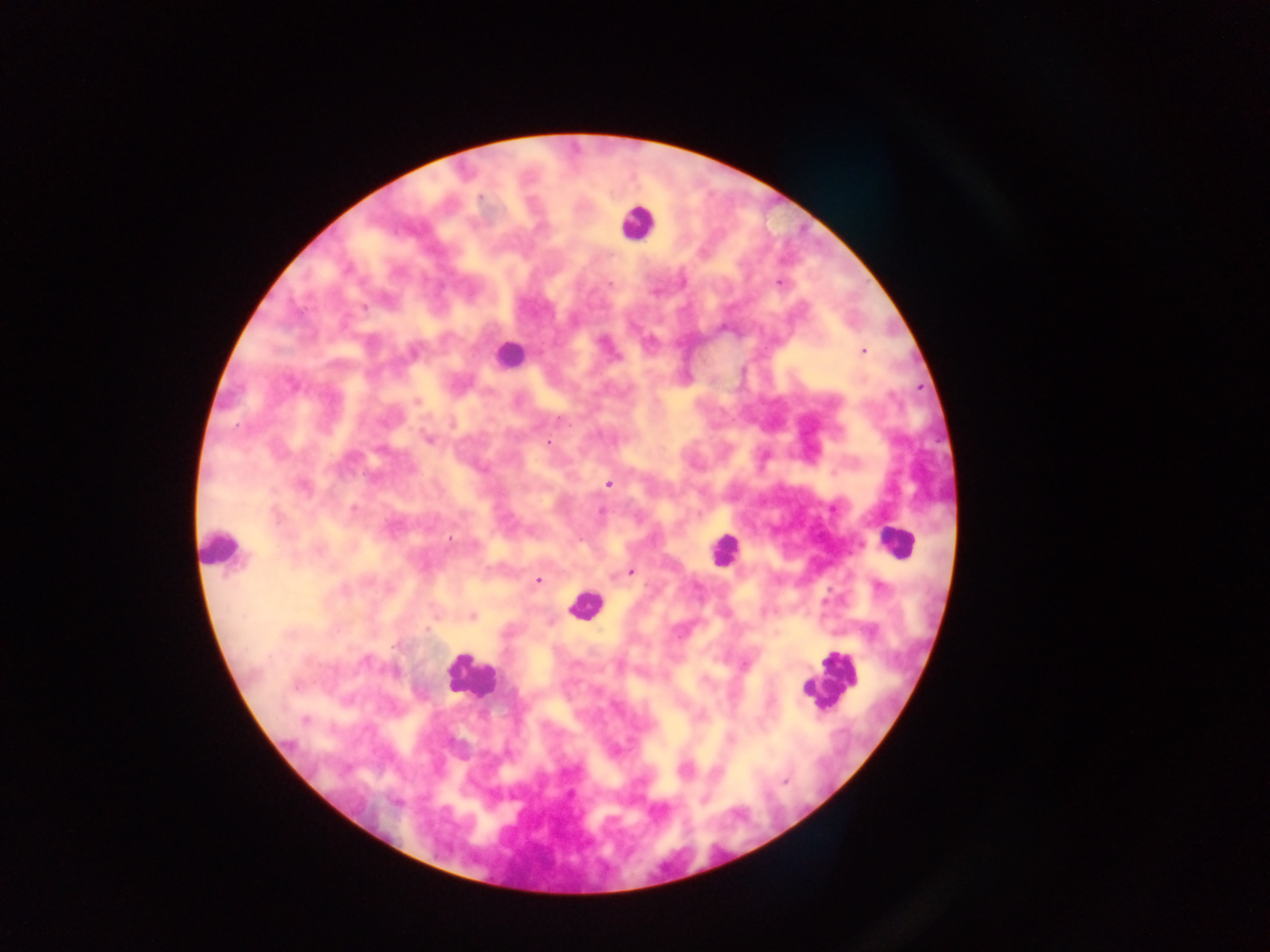

field of view = single
capture = mobile-phone photograph through a microscope
malaria parasite locations = approximate centers as x y in pixels: 480 197; 778 283; 610 284; 364 307; 863 351; 290 383; 417 401; 560 419; 428 439; 549 442; 608 484; 302 486; 353 508; 601 512; 450 538; 630 572; 537 580; 344 591; 472 617; 427 628; 366 660; 296 686; 772 702; 305 720; 731 738; 785 782; 394 803
preparation = thick blood smear
leukocyte locations = approximate centers as x y in pixels: 637 223; 508 354; 893 541; 220 548; 723 550; 585 605; 470 677; 831 678
country = Ghana
image size = 1270×952 pixels